Assess the morphology of the erythrocytes.
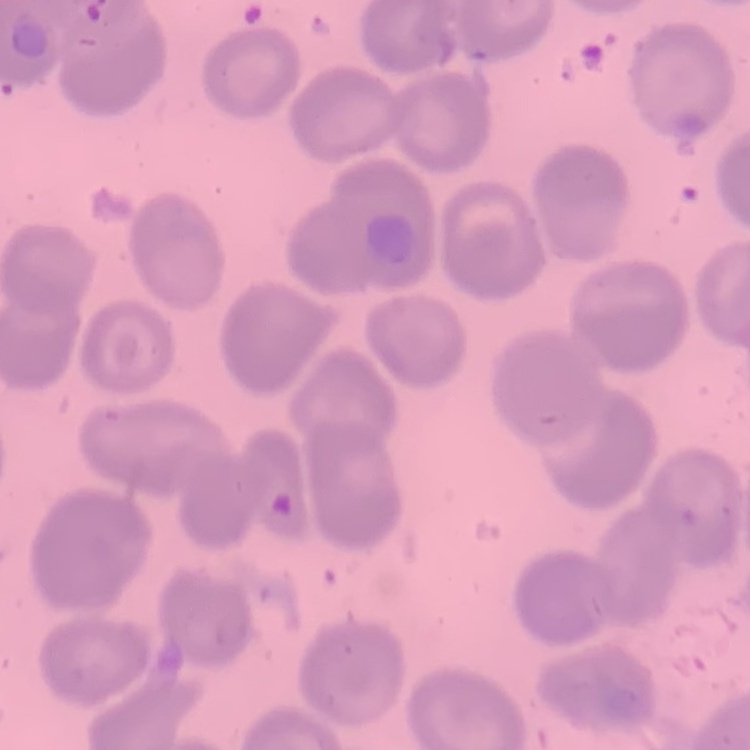
They show no rouleaux formation.

Thin blood film. Square crop of a larger photomicrograph. Stained with either Field's or Giemsa.